Outline each uninfected red blood cell.
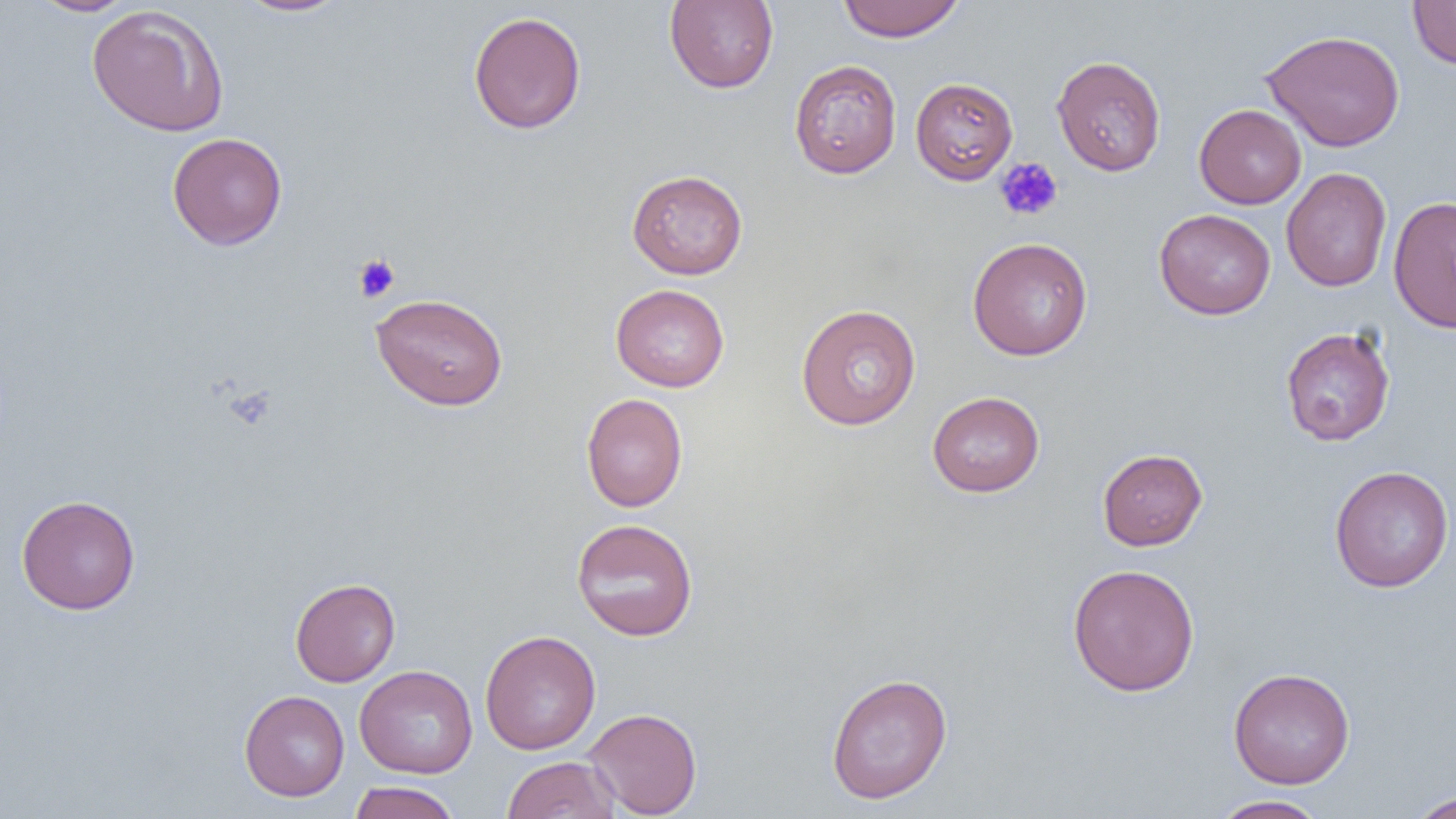

Approximate bounding boxes as (x1, y1, x2, y2) in pixels.
Uninfected red blood cells: (30, 0, 139, 16), (234, 0, 352, 17), (664, 0, 779, 93), (837, 0, 965, 42), (1407, 1, 1456, 69), (86, 5, 230, 137), (468, 11, 587, 134), (1261, 29, 1405, 152), (1051, 55, 1166, 176), (788, 59, 902, 178), (910, 77, 1018, 184), (1194, 104, 1306, 209), (167, 132, 288, 250), (1281, 167, 1392, 292), (626, 169, 748, 279), (1388, 195, 1456, 334), (1154, 208, 1276, 320), (967, 237, 1093, 360), (610, 284, 730, 392), (370, 292, 509, 411), (795, 303, 921, 431), (1280, 326, 1396, 446), (927, 391, 1045, 497), (581, 393, 688, 512), (1097, 448, 1207, 550), (1329, 465, 1454, 592), (15, 494, 141, 615), (571, 517, 699, 641), (1066, 563, 1200, 697), (289, 577, 401, 687), (480, 630, 601, 755), (354, 664, 477, 779), (1228, 667, 1355, 789), (825, 672, 953, 804), (239, 690, 350, 801), (583, 707, 703, 818), (502, 755, 620, 819), (348, 781, 461, 819), (1409, 791, 1456, 818), (1211, 795, 1330, 818).

Platelet locations: (994, 157, 1063, 222), (353, 254, 401, 302). Slide-level diagnosis: no evidence of blood parasites. One field of a larger specimen. Optical microscopy. Thin blood smear. Captured at 1000x magnification. Image is 1456×819 pixels.